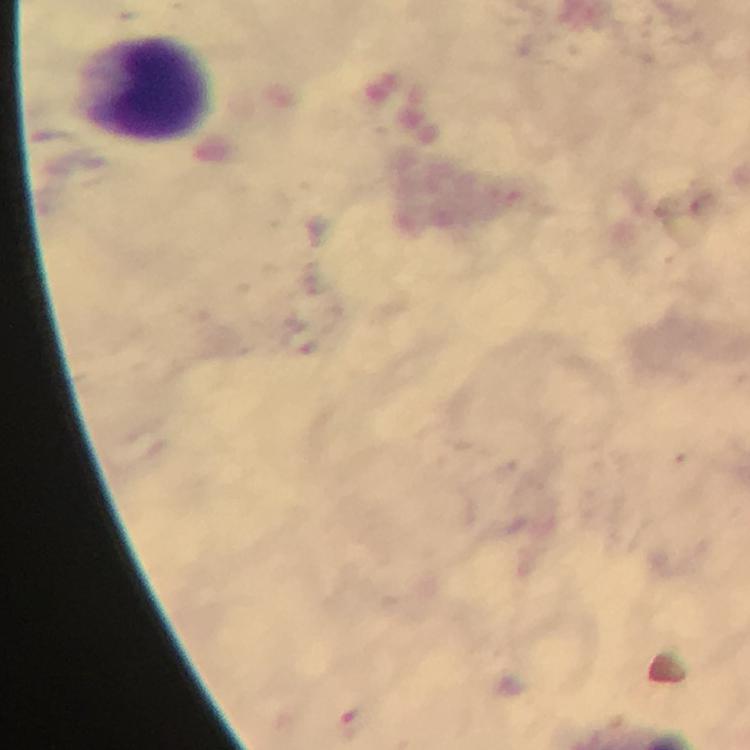
Approximate centers as [x, y] in pixels. Leukocyte locations: [145, 88]. Thick blood film. From a diagnostic examination for malaria. Immersion oil applied. Giemsa-stained preparation. Photographed through the microscope with a smartphone camera. At 100x magnification. Plasmodium parasites: none seen. Cropped region of a single field of view. Image is 750×750 pixels.